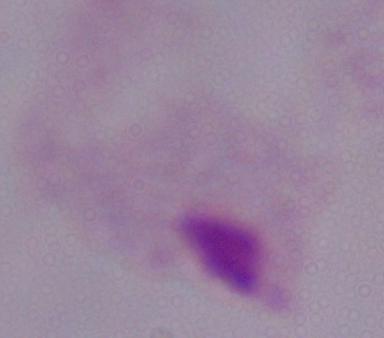

Photomicrograph. Captured at 1000x magnification. A trichomonad is shown.